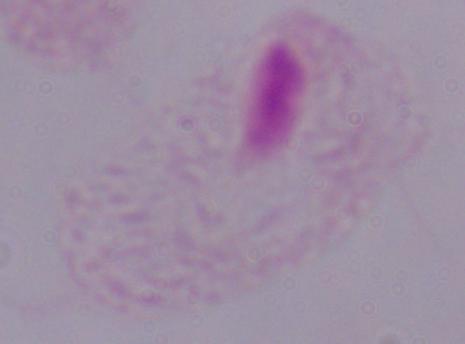

magnification = 1000x
identification = trichomonad
modality = micrograph